Identify the blood parasite species.
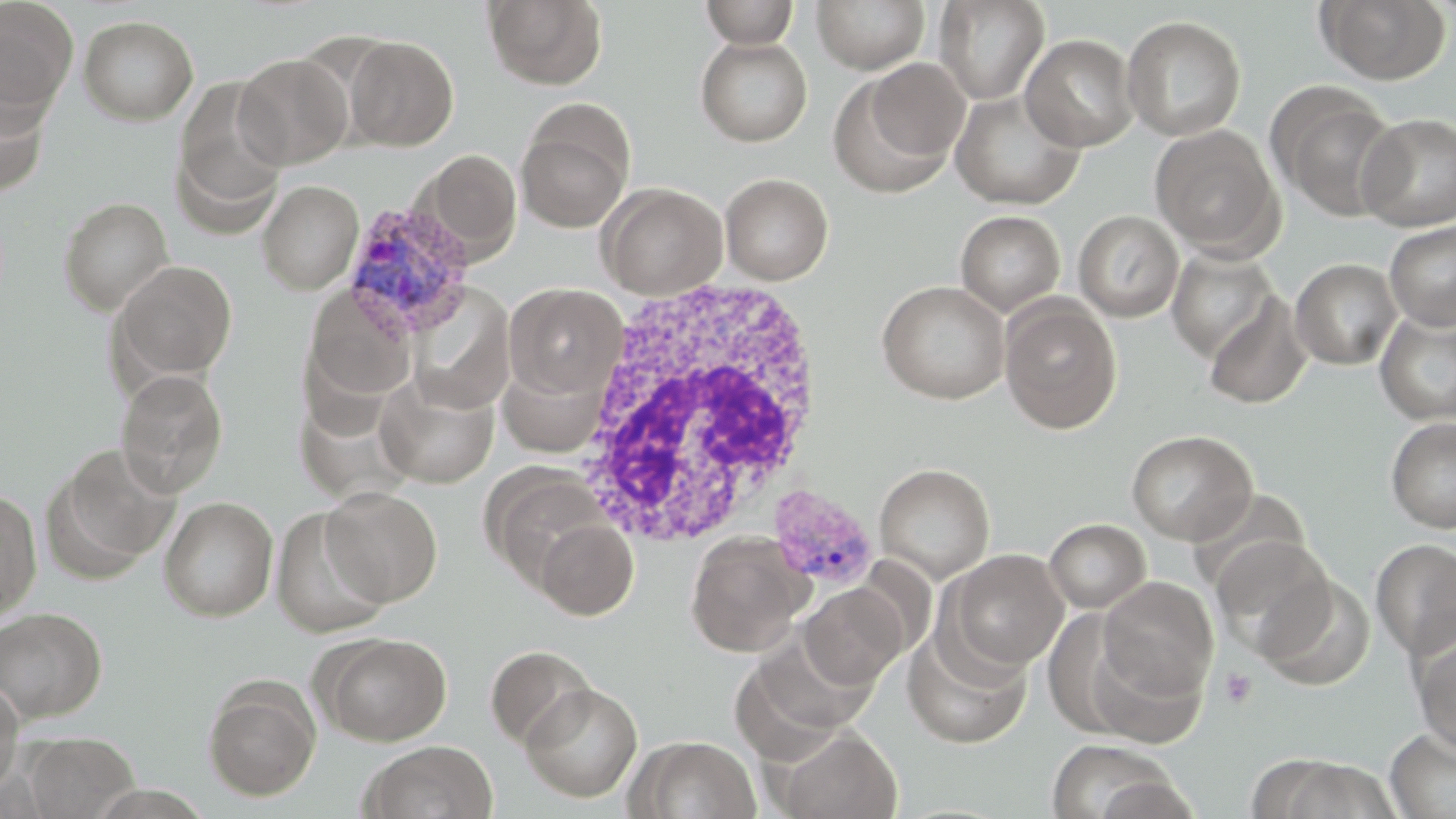
Plasmodium vivax.

Approximate bounding boxes as named x1/y1/x2/y2 corners in pixels. Plasmodium vivax-infected red blood cell locations: (x1=341, y1=201, x2=477, y2=341), (x1=767, y1=484, x2=880, y2=591). Uninfected red blood cell locations: (x1=484, y1=0, x2=607, y2=89), (x1=700, y1=0, x2=800, y2=48), (x1=811, y1=0, x2=930, y2=73), (x1=1316, y1=0, x2=1451, y2=84), (x1=0, y1=1, x2=78, y2=115), (x1=934, y1=1, x2=1049, y2=105), (x1=79, y1=15, x2=198, y2=124), (x1=1121, y1=15, x2=1247, y2=141), (x1=1020, y1=33, x2=1140, y2=152), (x1=343, y1=35, x2=458, y2=151), (x1=695, y1=36, x2=812, y2=147), (x1=234, y1=53, x2=353, y2=170), (x1=830, y1=61, x2=968, y2=197), (x1=170, y1=78, x2=290, y2=234), (x1=1269, y1=83, x2=1404, y2=222), (x1=0, y1=89, x2=50, y2=197), (x1=950, y1=90, x2=1085, y2=210), (x1=516, y1=102, x2=634, y2=234), (x1=1358, y1=113, x2=1456, y2=232), (x1=1149, y1=125, x2=1283, y2=256), (x1=418, y1=149, x2=522, y2=264), (x1=720, y1=173, x2=833, y2=284), (x1=257, y1=180, x2=363, y2=295), (x1=598, y1=182, x2=728, y2=299), (x1=58, y1=196, x2=174, y2=314), (x1=955, y1=210, x2=1066, y2=317), (x1=1073, y1=210, x2=1184, y2=322), (x1=1384, y1=221, x2=1456, y2=330), (x1=1166, y1=246, x2=1279, y2=363), (x1=1290, y1=258, x2=1402, y2=370), (x1=111, y1=260, x2=238, y2=384), (x1=876, y1=280, x2=1011, y2=404), (x1=505, y1=283, x2=627, y2=399), (x1=305, y1=286, x2=419, y2=401), (x1=1201, y1=292, x2=1313, y2=409), (x1=1000, y1=297, x2=1122, y2=434), (x1=1375, y1=307, x2=1456, y2=425), (x1=498, y1=359, x2=608, y2=458), (x1=116, y1=369, x2=229, y2=497), (x1=376, y1=372, x2=499, y2=488), (x1=1385, y1=416, x2=1456, y2=533), (x1=1126, y1=429, x2=1257, y2=546), (x1=46, y1=444, x2=179, y2=579), (x1=874, y1=463, x2=995, y2=584), (x1=495, y1=476, x2=613, y2=596), (x1=321, y1=486, x2=442, y2=606), (x1=0, y1=489, x2=42, y2=622), (x1=159, y1=496, x2=278, y2=621), (x1=270, y1=505, x2=392, y2=637), (x1=535, y1=518, x2=638, y2=620), (x1=1044, y1=518, x2=1151, y2=613), (x1=685, y1=532, x2=811, y2=657), (x1=1210, y1=537, x2=1335, y2=656), (x1=1370, y1=538, x2=1456, y2=660), (x1=946, y1=550, x2=1068, y2=672), (x1=1256, y1=574, x2=1376, y2=690), (x1=1098, y1=576, x2=1218, y2=700), (x1=799, y1=582, x2=910, y2=689), (x1=0, y1=606, x2=108, y2=724), (x1=902, y1=624, x2=1033, y2=749), (x1=316, y1=631, x2=451, y2=746), (x1=1413, y1=633, x2=1456, y2=756), (x1=485, y1=645, x2=596, y2=749), (x1=202, y1=676, x2=321, y2=801), (x1=0, y1=679, x2=24, y2=800), (x1=521, y1=682, x2=643, y2=802), (x1=772, y1=726, x2=902, y2=818), (x1=1384, y1=729, x2=1455, y2=818), (x1=23, y1=732, x2=138, y2=818), (x1=630, y1=735, x2=762, y2=818), (x1=1044, y1=739, x2=1181, y2=819), (x1=360, y1=740, x2=499, y2=819), (x1=1254, y1=756, x2=1404, y2=819). White blood cell locations: (x1=572, y1=271, x2=826, y2=552). Platelet locations: (x1=1219, y1=667, x2=1257, y2=709). Image is 1456×819 pixels. Optical microscopy. Captured at 1000x magnification. Single field of view. May-Grünwald-Giemsa-stained preparation. Thin blood smear.